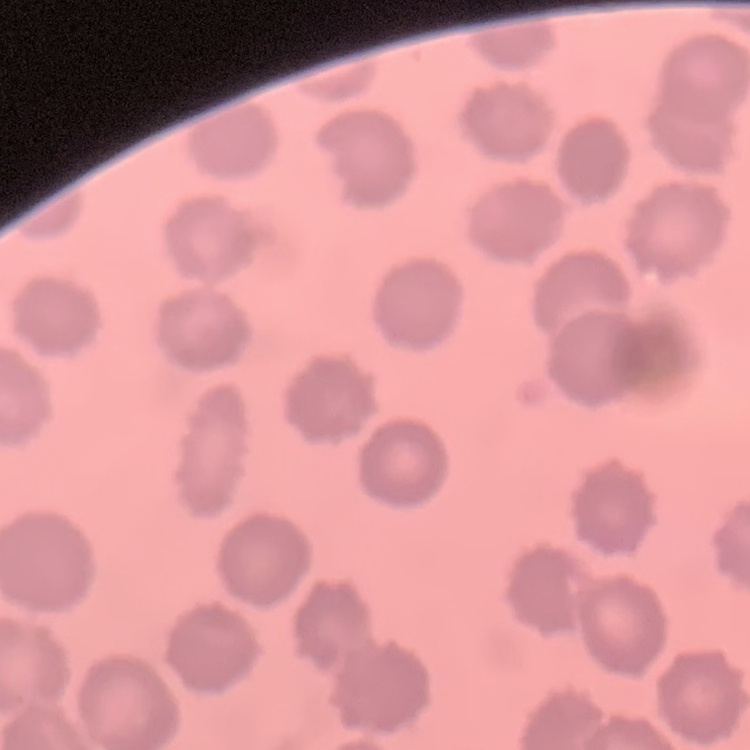
Summary:
  - Red blood cell morphology: no rouleaux formation
  - Stain: Field's or Giemsa
  - Preparation: thin blood smear
  - Image type: one tile cut from a larger photomicrograph